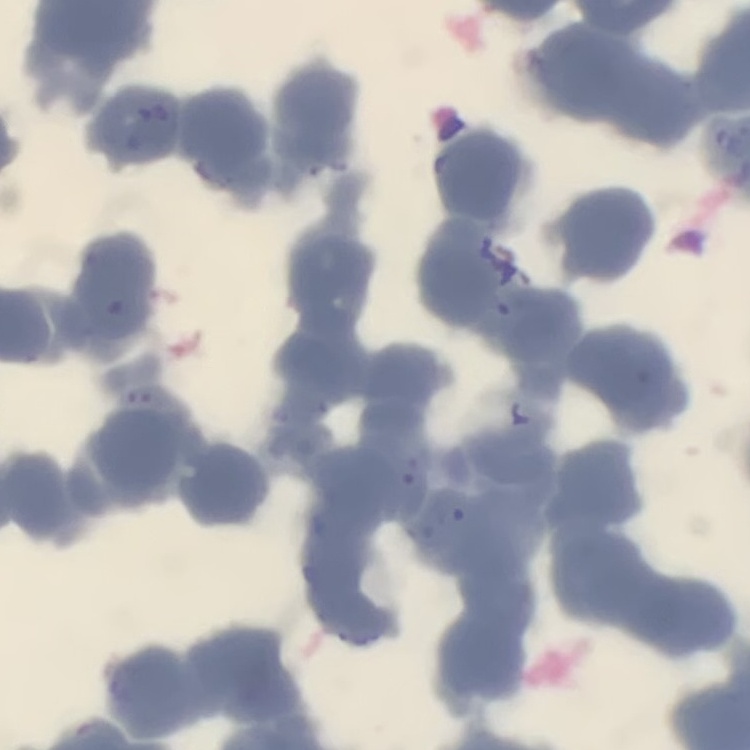
Summary:
  - Erythrocyte morphology: rouleaux formation
  - Stain: Field's or Giemsa
  - Image type: square crop of a larger photomicrograph
  - Preparation: thin blood smear